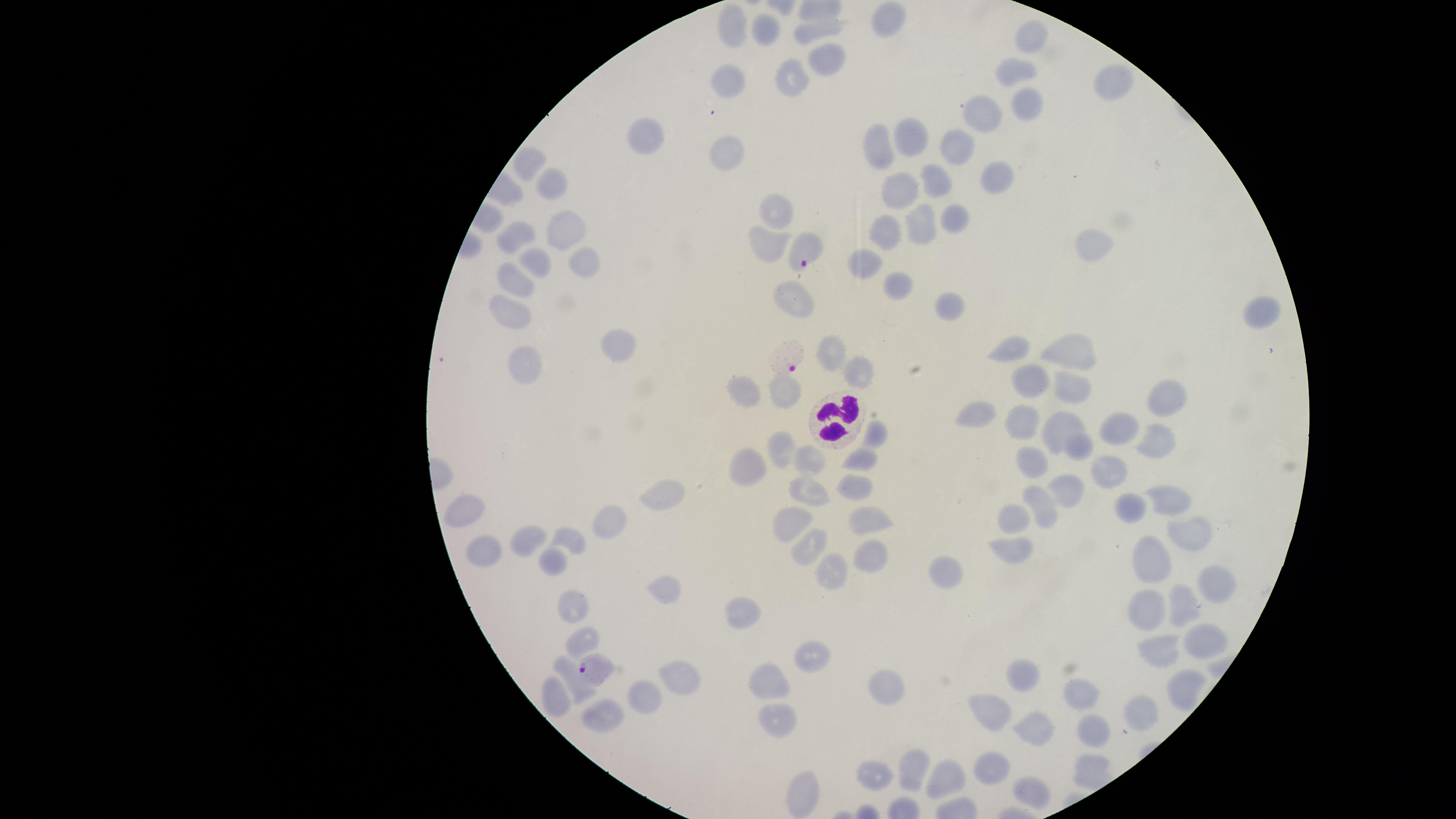

uninfected red blood cells = approximate marker points, in pixels from the top-left corner: (x=888, y=17), (x=730, y=21), (x=822, y=27), (x=766, y=31), (x=1034, y=38), (x=820, y=66), (x=1014, y=70), (x=792, y=76), (x=732, y=80), (x=1117, y=84), (x=1028, y=106), (x=985, y=116), (x=912, y=136), (x=645, y=137), (x=721, y=140), (x=879, y=147), (x=959, y=148), (x=529, y=165), (x=995, y=175), (x=933, y=178), (x=550, y=181), (x=900, y=189), (x=776, y=215), (x=954, y=221), (x=918, y=224), (x=886, y=226), (x=565, y=230), (x=518, y=235), (x=1096, y=247), (x=770, y=253), (x=582, y=258), (x=538, y=265), (x=868, y=267), (x=511, y=275), (x=900, y=282), (x=795, y=298), (x=942, y=299), (x=1253, y=312), (x=508, y=316), (x=619, y=344), (x=1008, y=344), (x=1072, y=349), (x=828, y=354), (x=519, y=358), (x=857, y=370), (x=1024, y=380), (x=745, y=389), (x=1066, y=390), (x=788, y=392), (x=1161, y=399), (x=977, y=413), (x=1023, y=421), (x=1062, y=426), (x=1126, y=429), (x=874, y=434), (x=1158, y=441), (x=779, y=444), (x=1074, y=448), (x=860, y=457), (x=809, y=459), (x=746, y=461), (x=1033, y=463), (x=1108, y=474), (x=855, y=486), (x=1063, y=490), (x=807, y=492), (x=662, y=495), (x=1132, y=498), (x=1169, y=500), (x=470, y=504), (x=1043, y=505), (x=1011, y=515), (x=609, y=522), (x=863, y=525), (x=783, y=529), (x=527, y=536), (x=1196, y=537), (x=575, y=541), (x=1012, y=547), (x=484, y=548), (x=809, y=548), (x=553, y=554), (x=870, y=555), (x=1151, y=557), (x=829, y=565), (x=947, y=570), (x=1225, y=581), (x=665, y=588), (x=1183, y=602), (x=577, y=609), (x=747, y=610), (x=1153, y=610), (x=1205, y=636), (x=584, y=639), (x=809, y=652), (x=1161, y=652), (x=1019, y=673), (x=687, y=680), (x=773, y=681), (x=888, y=682), (x=1182, y=687), (x=579, y=691), (x=648, y=694), (x=1080, y=696), (x=552, y=698), (x=601, y=712), (x=991, y=712), (x=1136, y=713), (x=777, y=714), (x=1031, y=731), (x=1090, y=735), (x=915, y=770), (x=997, y=771), (x=869, y=777), (x=946, y=778), (x=1029, y=792)
field of view = single
species = Plasmodium falciparum
visible region = circular
presence = malaria parasites seen
image size = 1456×819 pixels
preparation = thin smear of blood
parasitized red blood cells = approximate marker points, in pixels from the top-left corner: (x=805, y=250), (x=789, y=356), (x=595, y=668)
stain = Giemsa
capture = smartphone photograph through the microscope eyepiece
white blood cells = approximate marker points, in pixels from the top-left corner: (x=830, y=418)